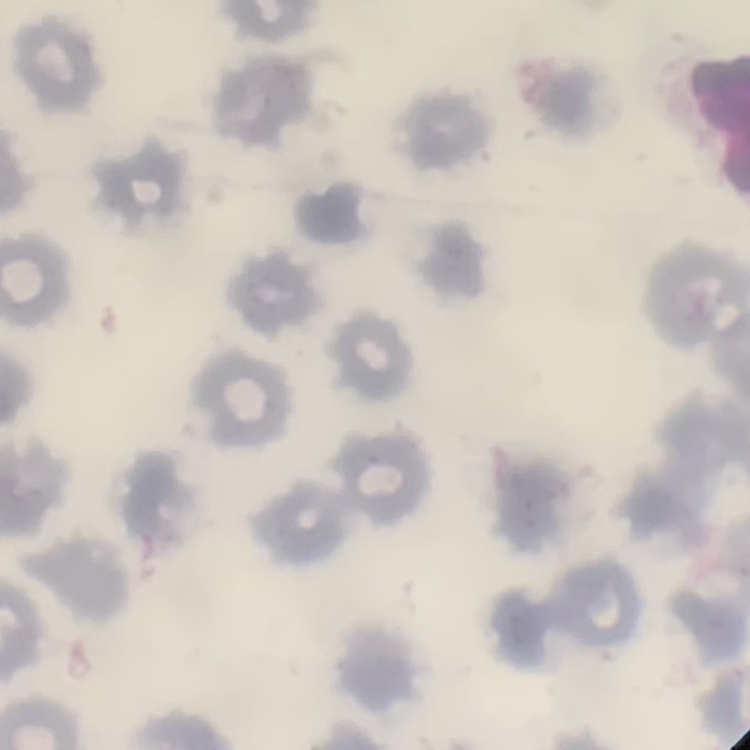
The erythrocytes show no rouleaux formation. One tile cut from a larger photomicrograph. Field's or Giemsa stain. Thin blood film.